Assess this cell for malaria.
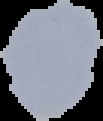

Uninfected.

Image is 103×121 pixels. From a thin blood film. The area outside the segmented cell region is set to black.